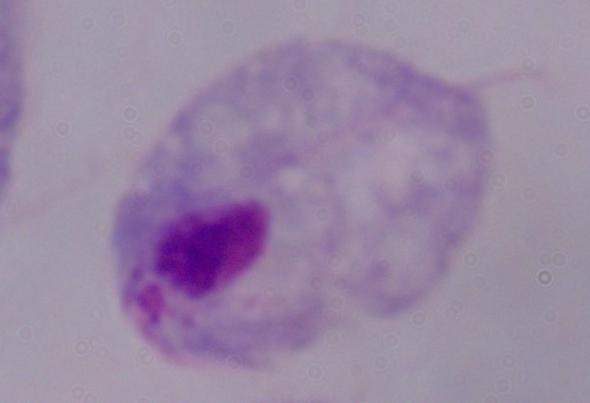

Summary:
  - Magnification: 1000x
  - Identification: trichomonad
  - Modality: micrograph